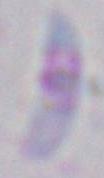 Toxoplasma gondii is seen. Micrograph. 1000x magnification.